State which parasite is depicted.
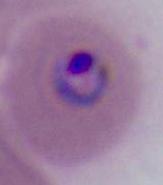

Plasmodium.

{
  "magnification": "400x or 1000x",
  "modality": "micrograph"
}